State which cell type is depicted.
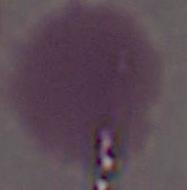
This is an erythrocyte.

Summary:
  - Modality: photomicrograph
  - Magnification: 1000x